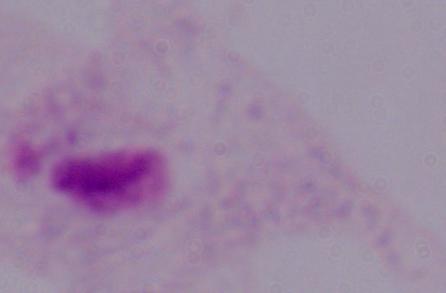
magnification = 1000x
modality = micrograph
identification = trichomonad